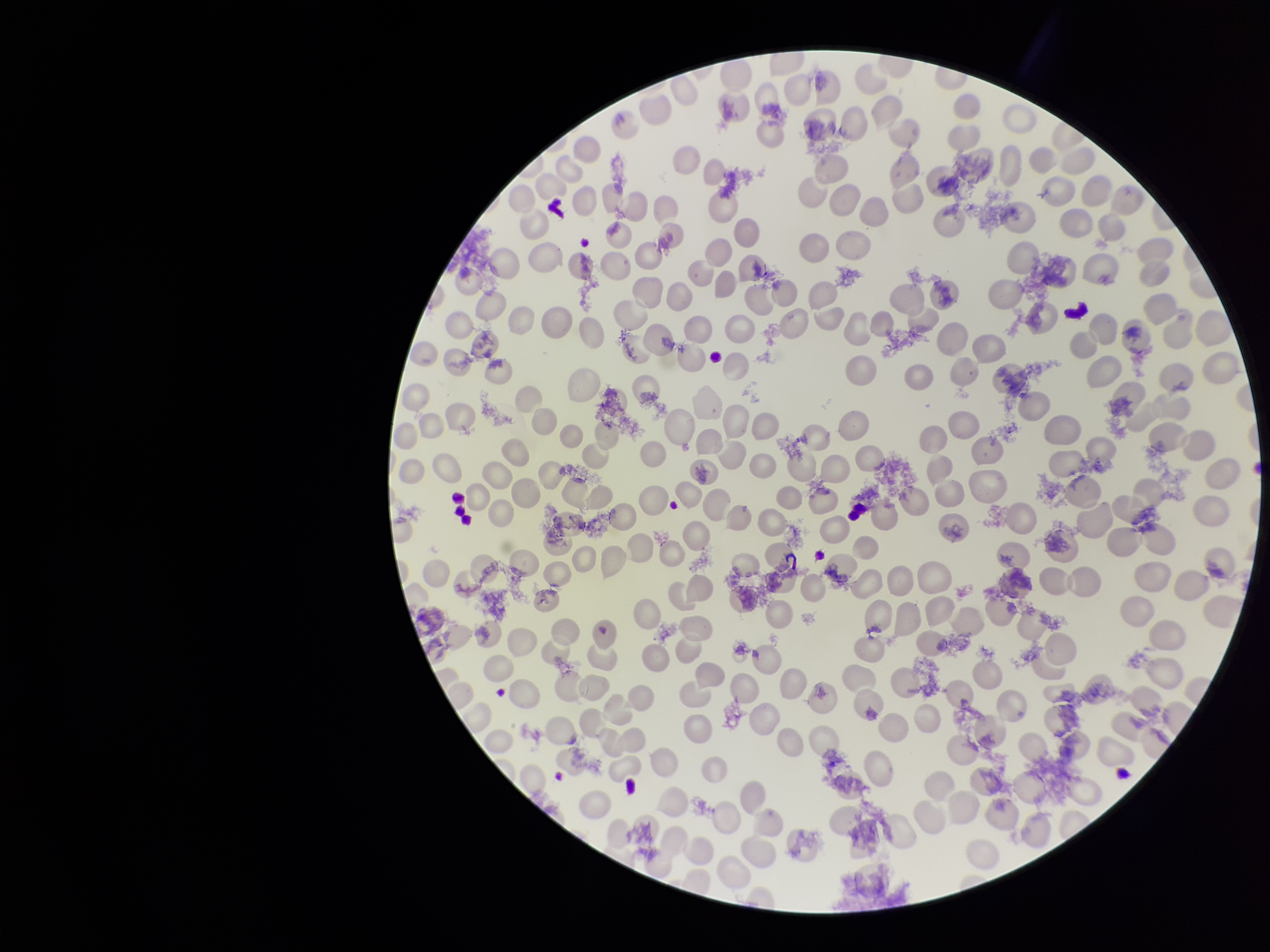

Single field of view. Preparation: thin. Smartphone photograph taken through the eyepiece of a microscope. Parasitized red blood cell count: 0. Patient malaria status: negative. Stained with Giemsa. Red blood cell count: 263. Parasitized red blood cells: none seen. Image is 1270×952 pixels.